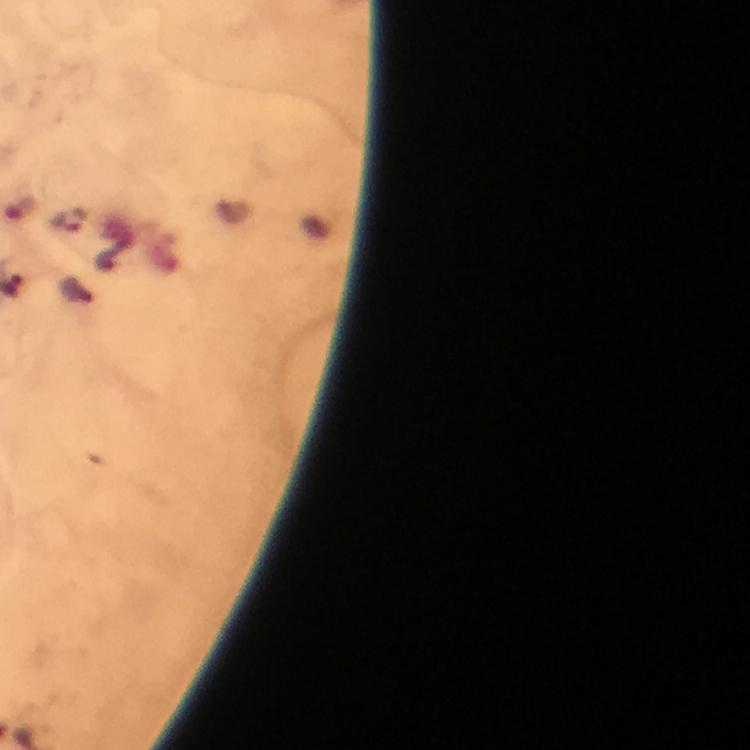
capture = smartphone camera through the microscope
stain = Giemsa
cropped from = a single field of view
preparation = thick smear
magnification = 100x
Plasmodium parasite locations = approximate centers as {x, y} in pixels: {71, 219}
context = from a malaria diagnostic workup
immersion oil = used
image size = 750×750 pixels